Outline each uninfected red blood cell.
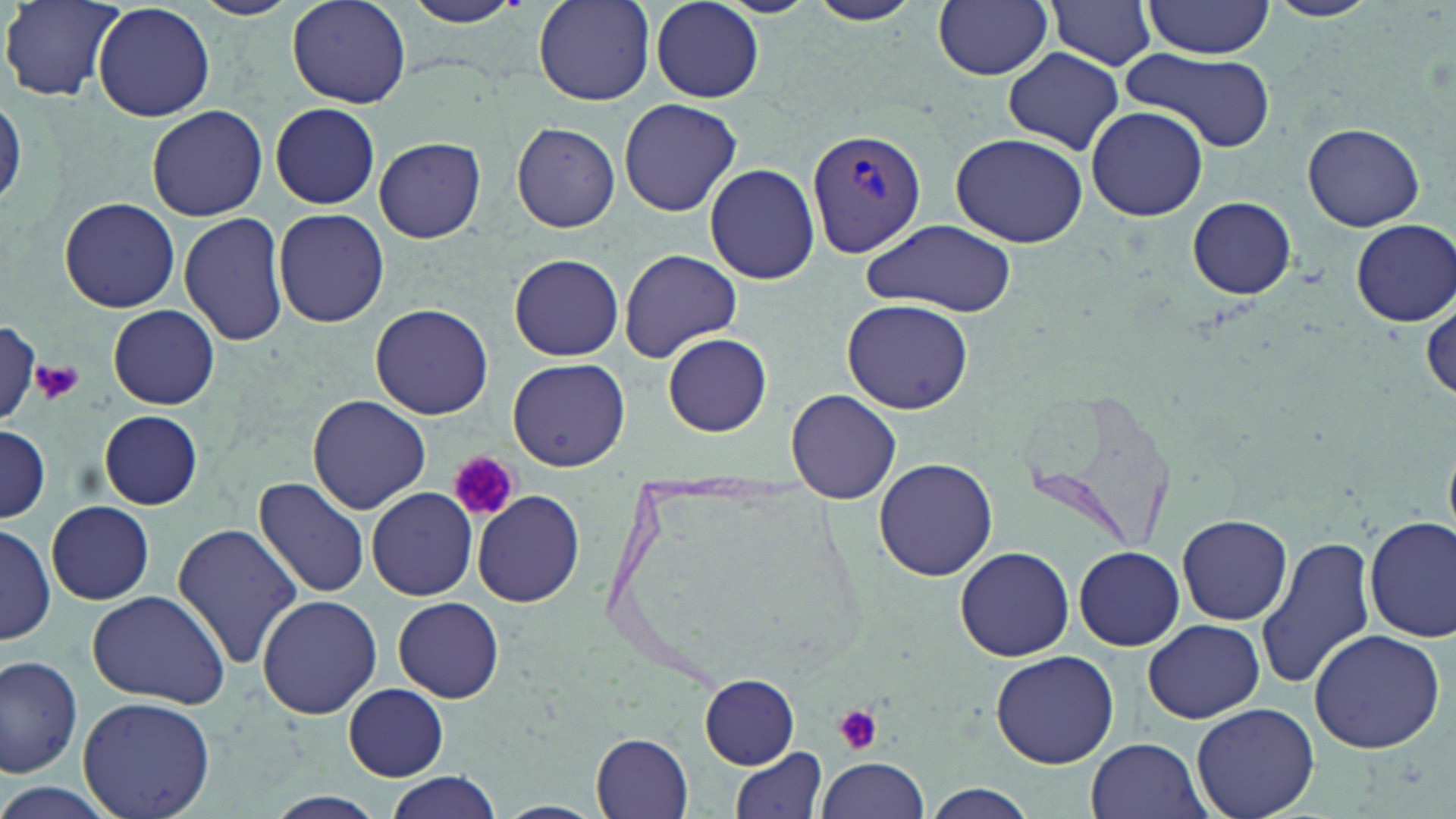
Approximate bounding boxes as (x1,y1)-(x2,y2) corner pairs in pixels.
Uninfected red blood cells: (191,0)-(300,19), (288,0)-(411,109), (397,0)-(531,28), (532,0)-(654,105), (803,0)-(926,27), (932,0)-(1053,80), (1044,0)-(1160,70), (1264,0)-(1382,23), (2,1)-(120,100), (650,1)-(764,102), (1141,1)-(1279,63), (92,2)-(216,122), (1003,48)-(1125,157), (1119,48)-(1279,154), (0,93)-(24,215), (619,99)-(742,216), (268,103)-(381,208), (147,106)-(268,220), (1083,107)-(1206,222), (510,121)-(621,234), (1303,122)-(1424,231), (948,133)-(1089,247), (374,137)-(486,243), (703,163)-(819,284), (60,196)-(181,312), (1187,197)-(1296,300), (272,208)-(390,327), (178,211)-(289,347), (1351,218)-(1455,326), (861,219)-(1017,315), (619,248)-(743,362), (509,253)-(624,361), (843,299)-(973,414), (370,303)-(493,420), (109,305)-(219,409), (0,325)-(43,418), (663,332)-(772,437), (507,357)-(630,472), (787,389)-(901,503), (1025,391)-(1175,555), (306,396)-(432,514), (98,409)-(202,510), (0,426)-(48,525), (874,458)-(998,580), (253,475)-(371,599), (367,485)-(480,602), (472,490)-(588,608), (47,501)-(154,605), (1178,512)-(1293,624), (1365,517)-(1455,643), (0,522)-(55,644), (170,522)-(301,669), (1257,534)-(1377,690), (955,545)-(1075,662), (1074,546)-(1185,651), (86,589)-(230,710), (255,594)-(381,719), (393,597)-(504,703), (1143,618)-(1265,724), (1308,628)-(1445,754), (990,649)-(1120,769), (0,652)-(83,780), (701,675)-(799,767), (344,683)-(448,780), (77,696)-(216,819), (1192,702)-(1320,819), (592,732)-(694,816), (1086,736)-(1210,819), (730,745)-(827,819), (819,756)-(930,819), (384,773)-(504,819), (0,781)-(124,819), (920,787)-(1040,819).

{
  "slide_level_diagnosis": "Plasmodium vivax",
  "platelet_locations": "approximate bounding boxes as (x1,y1)-(x2,y2) corner pairs in pixels: (33,361)-(83,404), (450,453)-(519,523), (831,702)-(884,756)",
  "field_of_view": "single",
  "preparation": "thin blood film",
  "plasmodium_vivax_infected_red_blood_cell_locations": "approximate bounding boxes as (x1,y1)-(x2,y2) corner pairs in pixels: (807,127)-(925,257)",
  "magnification": "1000x",
  "modality": "light microscopy",
  "image_size": "1456×819 pixels",
  "stain": "May-Grünwald-Giemsa"
}